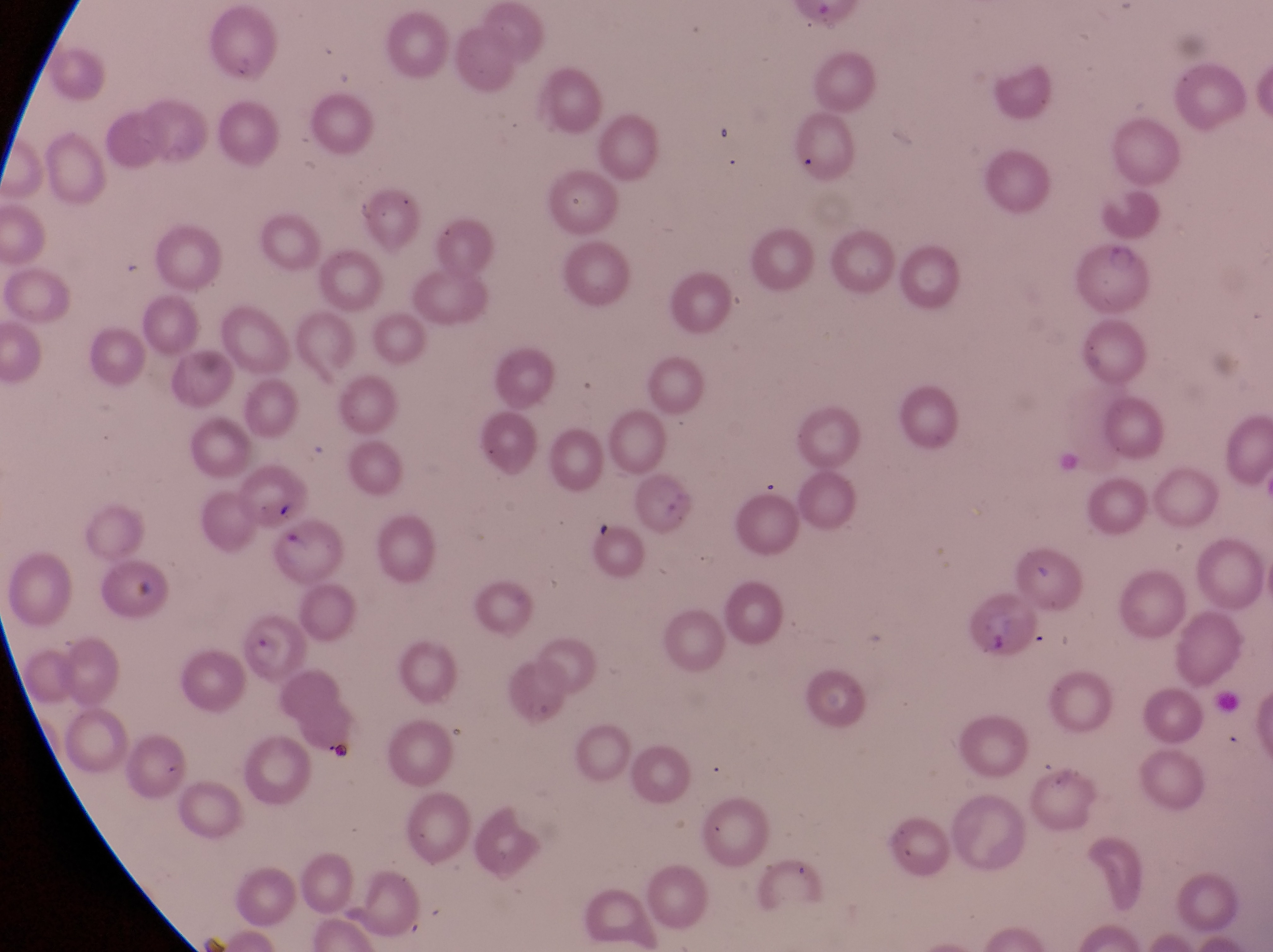

magnification = 1000x
artifact (platelet-like body, stain precipitate, or debris) locations = approximate bounding boxes as left top right bottom in pixels: 127 574 169 602
capture = smartphone photograph through the eyepiece of an Olympus CX-23 microscope
image size = 1273×952 pixels
preparation = thin blood film
field of view = single
parasitised red blood cell locations = approximate bounding boxes as left top right bottom in pixels: 964 599 1041 669; 237 621 302 686
country = Uganda